Give the position of every malaria parasite.
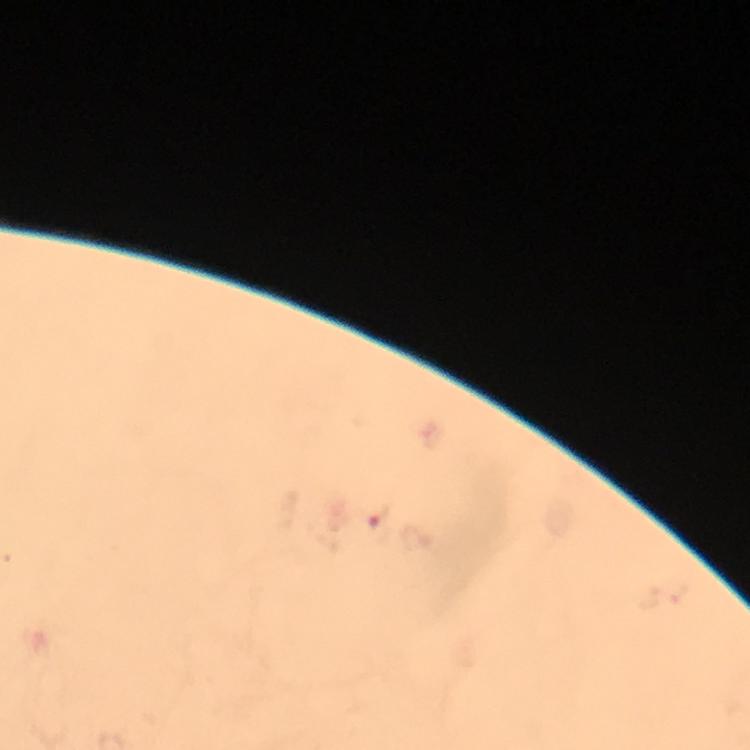

Approximate centers as [x, y] in pixels.
Malaria parasites: [377, 525].

Cropped region of a single field of view. Thick blood smear. Image is 750×750 pixels. Smartphone photograph taken through a microscope. Giemsa-stained preparation. Immersion oil applied. 100x magnification. From a malaria diagnostic workup.